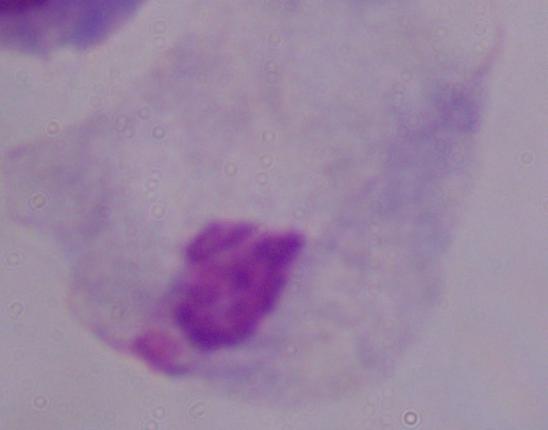
modality: photomicrograph
magnification: 1000x
identification: trichomonad